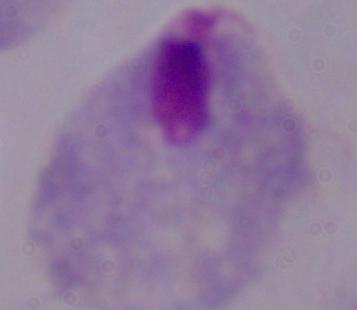
A trichomonad is shown. Photomicrograph. 1000x magnification.